Report the malaria status of this cell.
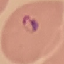
It is parasitized.

preparation = thin blood smear
image type = cell patch, automatically extracted from a larger field of view and resized to 64 × 64 pixels
stain = Giemsa
capture = smartphone through the microscope eyepiece